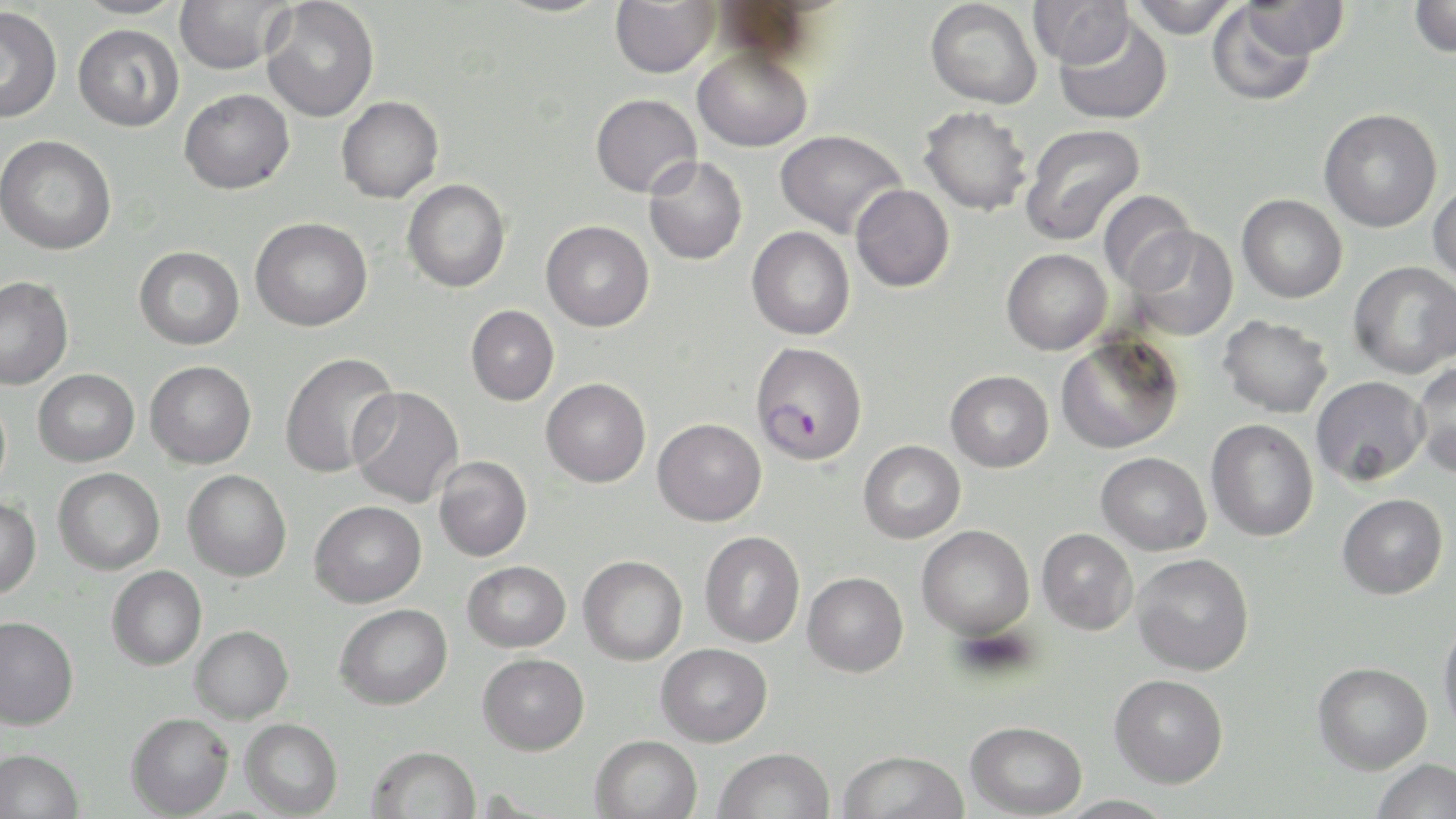
{
  "slide_level_diagnosis": "Plasmodium falciparum",
  "stain": "May-Grünwald-Giemsa",
  "preparation": "thin blood smear",
  "plasmodium_falciparum_infected_red_blood_cell_locations": "approximate bounding boxes as [x1, y1, x2, y2] in pixels: [749, 341, 867, 465]",
  "magnification": "1000x",
  "modality": "light microscopy",
  "uninfected_red_blood_cell_locations": "approximate bounding boxes as [x1, y1, x2, y2] in pixels: [71, 0, 188, 19], [174, 0, 291, 75], [261, 0, 379, 122], [493, 0, 613, 18], [610, 0, 720, 78], [925, 0, 1042, 109], [1029, 0, 1134, 68], [1129, 0, 1239, 39], [1409, 0, 1456, 58], [1239, 1, 1349, 59], [1207, 2, 1321, 106], [0, 6, 62, 123], [1054, 14, 1172, 125], [73, 23, 184, 132], [692, 46, 813, 152], [179, 89, 294, 194], [590, 93, 702, 197], [336, 96, 443, 203], [918, 106, 1033, 216], [1318, 108, 1442, 232], [1021, 123, 1146, 247], [774, 129, 907, 238], [0, 135, 116, 255], [644, 156, 748, 265], [402, 179, 511, 293], [1428, 181, 1456, 284], [851, 184, 954, 292], [1098, 190, 1197, 292], [1236, 194, 1347, 303], [250, 217, 372, 331], [541, 220, 654, 332], [747, 226, 855, 340], [1125, 226, 1238, 341], [134, 245, 244, 349], [1002, 249, 1112, 355], [1349, 261, 1456, 379], [0, 276, 73, 390], [466, 305, 559, 406], [1218, 315, 1333, 418], [1055, 332, 1185, 455], [280, 351, 401, 478], [145, 360, 256, 468], [1412, 360, 1456, 477], [33, 369, 139, 466], [945, 370, 1054, 472], [1311, 375, 1429, 486], [541, 378, 651, 487], [348, 386, 464, 506], [653, 418, 767, 526], [1206, 419, 1319, 541], [858, 440, 966, 543], [1096, 452, 1212, 555], [434, 456, 532, 561], [53, 468, 165, 575], [183, 470, 291, 581], [1337, 493, 1448, 599], [0, 495, 41, 598], [310, 501, 426, 607], [917, 525, 1034, 640], [1036, 528, 1138, 635], [699, 531, 805, 647], [1132, 553, 1254, 675], [578, 555, 687, 665], [462, 560, 571, 652], [107, 566, 207, 670], [802, 572, 908, 677], [335, 603, 452, 709], [0, 615, 79, 730], [1438, 615, 1456, 740], [190, 625, 293, 723], [656, 643, 772, 746], [478, 653, 589, 755], [1313, 661, 1432, 774], [1109, 674, 1228, 788], [126, 712, 234, 817], [240, 718, 342, 818], [966, 720, 1087, 818], [590, 734, 703, 819], [366, 745, 481, 819], [714, 747, 835, 819], [0, 748, 84, 819], [836, 748, 970, 819], [1371, 758, 1455, 819], [1054, 795, 1180, 818]",
  "field_of_view": "single",
  "image_size": "1456×819 pixels"
}